Outline each blood parasite and name the species.
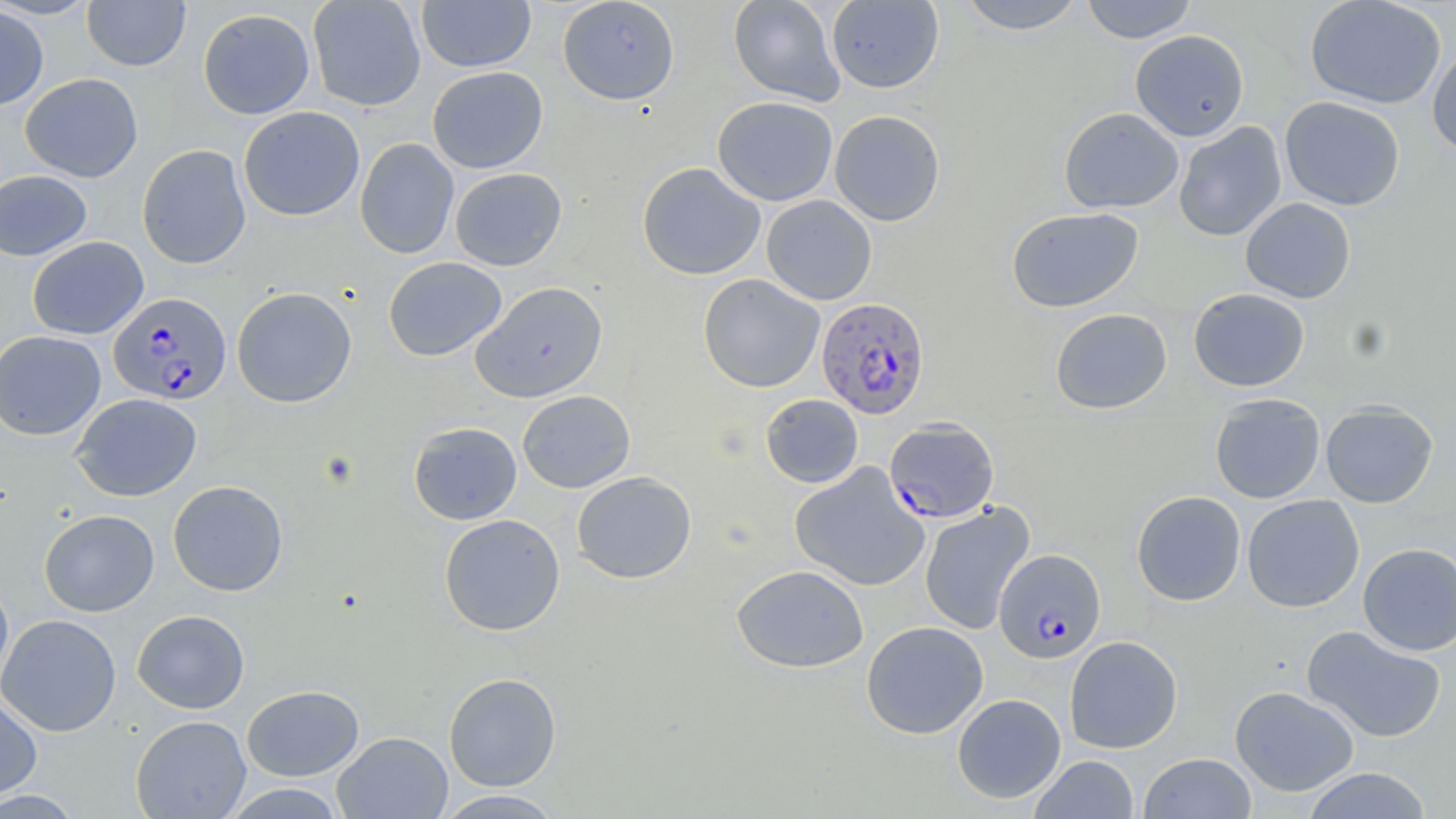
Approximate bounding boxes as [x1, y1, x2, y2] in pixels.
Plasmodium falciparum-infected red blood cells: [108, 291, 232, 405], [815, 296, 930, 419], [884, 417, 1000, 523], [994, 548, 1106, 663].
No Plasmodium ovale, Plasmodium malariae, Plasmodium vivax, Babesia divergens, or Trypanosoma brucei observed.

{
  "slide_level_diagnosis": "Plasmodium falciparum",
  "modality": "light microscopy",
  "uninfected_red_blood_cell_locations": "approximate bounding boxes as [x1, y1, x2, y2] in pixels: [0, 0, 101, 20], [82, 0, 190, 72], [307, 0, 426, 111], [416, 0, 536, 72], [557, 0, 680, 105], [728, 0, 845, 106], [955, 0, 1086, 34], [1080, 0, 1198, 44], [1304, 0, 1447, 109], [826, 1, 944, 93], [0, 4, 49, 110], [197, 8, 315, 120], [1130, 29, 1249, 141], [1427, 43, 1456, 159], [427, 66, 548, 173], [20, 73, 143, 182], [712, 96, 838, 206], [1279, 96, 1406, 211], [239, 106, 365, 222], [1059, 107, 1184, 214], [829, 109, 946, 226], [1173, 121, 1287, 241], [355, 138, 459, 259], [137, 144, 251, 269], [637, 162, 765, 280], [449, 168, 567, 271], [0, 170, 92, 261], [761, 195, 877, 305], [1240, 197, 1356, 303], [1007, 207, 1143, 313], [27, 236, 148, 340], [383, 257, 507, 361], [698, 273, 825, 393], [471, 281, 609, 403], [231, 287, 357, 408], [1188, 287, 1310, 392], [1050, 308, 1172, 413], [1, 330, 106, 441], [517, 390, 635, 493], [71, 393, 202, 501], [760, 394, 863, 488], [1209, 396, 1325, 505], [1320, 400, 1439, 508], [408, 421, 522, 525], [790, 462, 930, 592], [571, 471, 696, 584], [168, 480, 288, 596], [1131, 490, 1246, 606], [1242, 494, 1365, 612], [920, 501, 1035, 635], [39, 509, 159, 616], [439, 514, 565, 636], [1358, 542, 1456, 655], [731, 564, 868, 673], [0, 577, 14, 696], [132, 609, 250, 714], [0, 613, 122, 737], [861, 621, 988, 739], [1301, 625, 1446, 743], [1064, 635, 1182, 753], [443, 672, 561, 791], [241, 685, 364, 781], [1229, 685, 1359, 796], [952, 693, 1066, 803], [0, 694, 43, 803], [131, 715, 251, 818], [332, 731, 453, 818], [1139, 752, 1256, 819], [1029, 755, 1139, 818], [1301, 767, 1433, 818], [221, 783, 349, 818], [433, 789, 567, 818], [0, 790, 86, 817]",
  "image_size": "1456×819 pixels",
  "magnification": "1000x",
  "field_of_view": "single",
  "stain": "May-Grünwald-Giemsa",
  "preparation": "thin blood smear"
}